Describe the morphology of the erythrocytes.
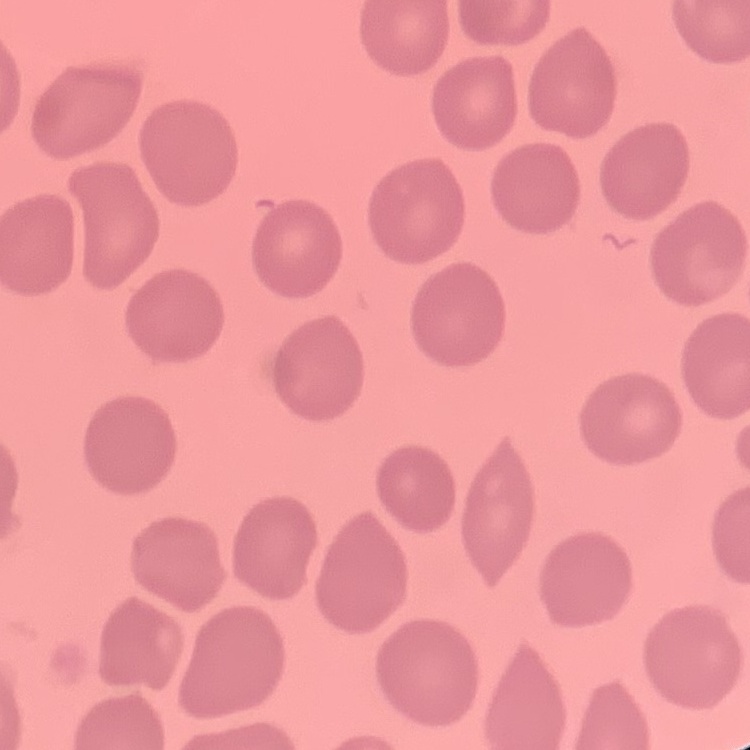

They show no rouleaux formation.

Thin peripheral smear. Square crop of a larger photomicrograph. Stained with either Field's or Giemsa.